Locate every uninfected red blood cell.
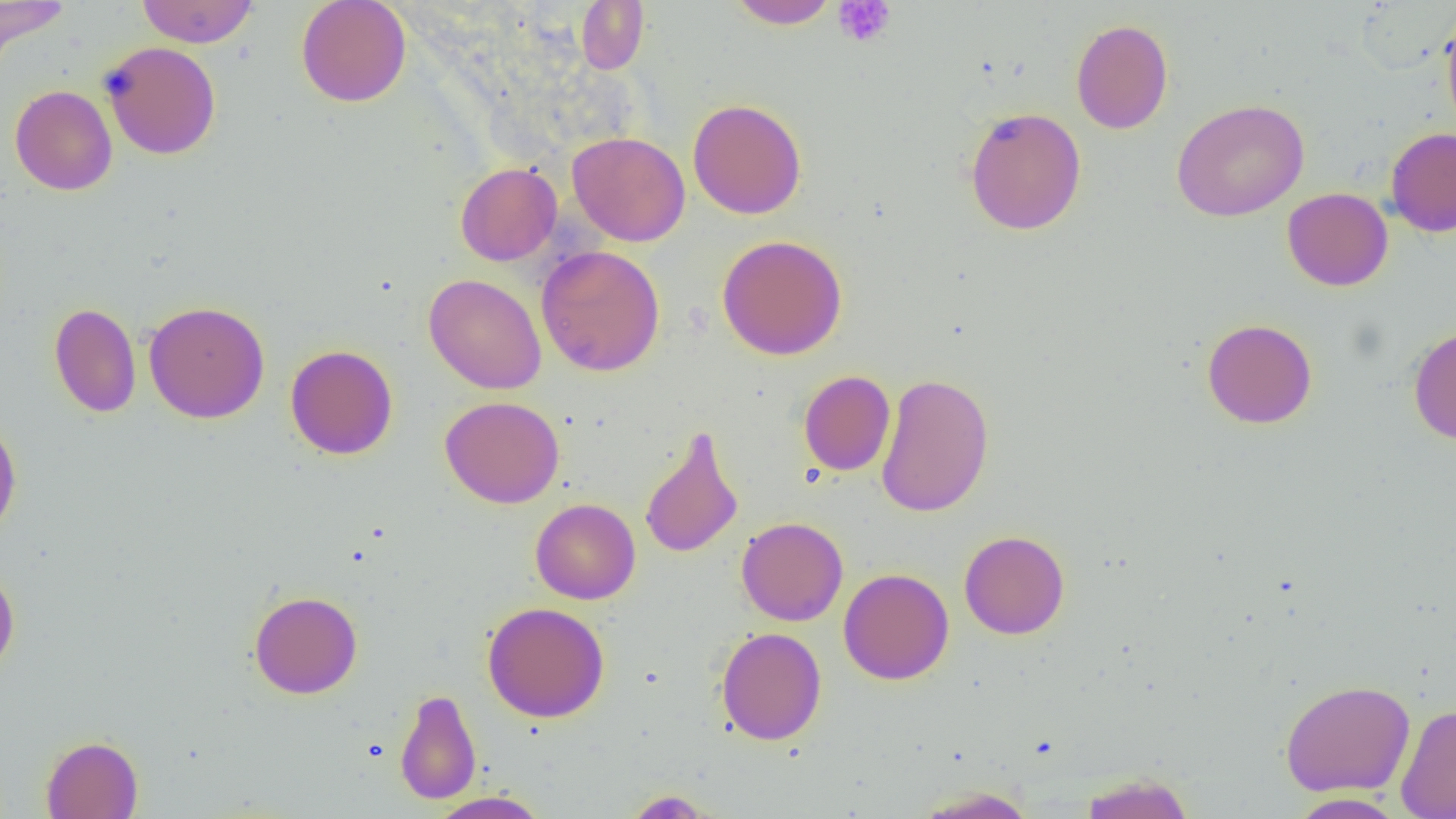
Approximate bounding boxes as (x1, y1, x2, y2) in pixels.
Uninfected red blood cells: (0, 0, 70, 64), (136, 0, 259, 47), (296, 0, 412, 107), (727, 0, 840, 29), (575, 1, 649, 74), (1440, 11, 1456, 138), (1071, 19, 1173, 134), (100, 41, 221, 160), (10, 85, 117, 195), (687, 98, 807, 219), (1172, 99, 1309, 221), (964, 107, 1086, 236), (1386, 127, 1456, 238), (568, 132, 690, 246), (455, 163, 561, 266), (1282, 187, 1393, 291), (717, 235, 848, 360), (536, 245, 666, 377), (424, 273, 547, 395), (144, 300, 270, 424), (49, 302, 141, 418), (1202, 318, 1317, 429), (1408, 326, 1456, 445), (285, 344, 398, 460), (799, 370, 896, 476), (875, 372, 995, 518), (440, 395, 565, 508), (0, 413, 22, 540), (639, 426, 744, 559), (531, 498, 641, 604), (736, 517, 848, 626), (959, 530, 1070, 639), (0, 564, 20, 679), (838, 568, 954, 685), (249, 591, 363, 698), (482, 601, 610, 723), (716, 627, 827, 745), (1280, 679, 1415, 796), (395, 688, 482, 805), (1396, 704, 1456, 819), (40, 735, 143, 818), (1078, 773, 1195, 818), (913, 786, 1036, 818), (621, 789, 719, 817), (429, 791, 550, 819), (1288, 792, 1406, 818).

Summary:
  - Platelet locations: (833, 1, 896, 47)
  - Slide-level diagnosis: no evidence of blood parasites
  - Image size: 1456×819 pixels
  - Magnification: 1000x
  - Modality: optical microscopy
  - Preparation: thin blood smear
  - Field of view: single